State which parasite is depicted.
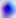
Toxoplasma gondii.

Photomicrograph. Captured at 400x magnification.